Describe the morphology of the red blood cells.
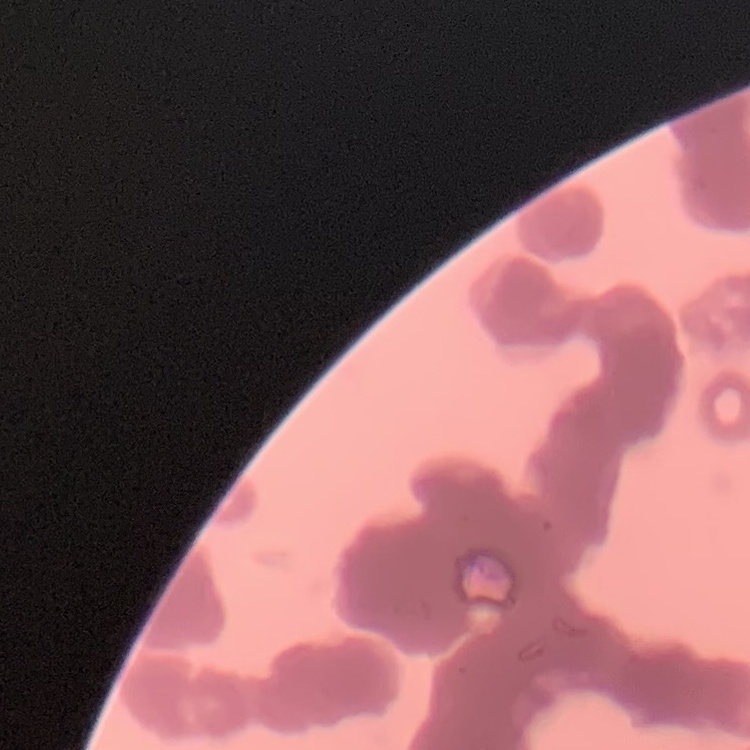

They show rouleaux formation.

Thin blood smear. Field's or Giemsa stain. One tile cut from a larger photomicrograph.